Locate every Plasmodium parasite.
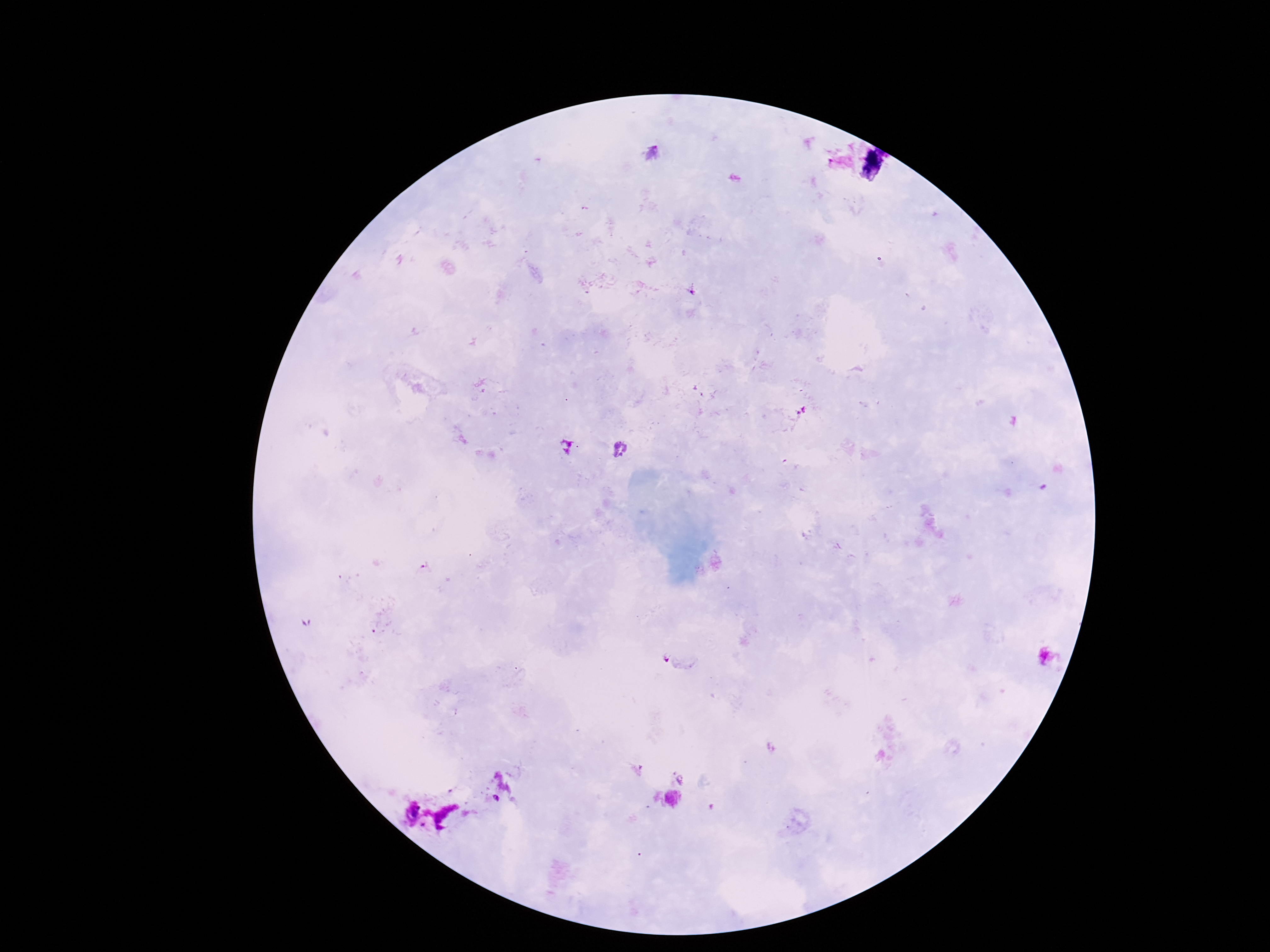

Approximate centers as [x, y] in pixels.
Plasmodium parasites: [621, 450], [664, 656].

preparation: thick blood film
image_size: 1270×952 pixels
magnification: 100x
capture: smartphone camera through the microscope eyepiece
patient_malaria_status: positive
field_of_view: single
stain: Giemsa